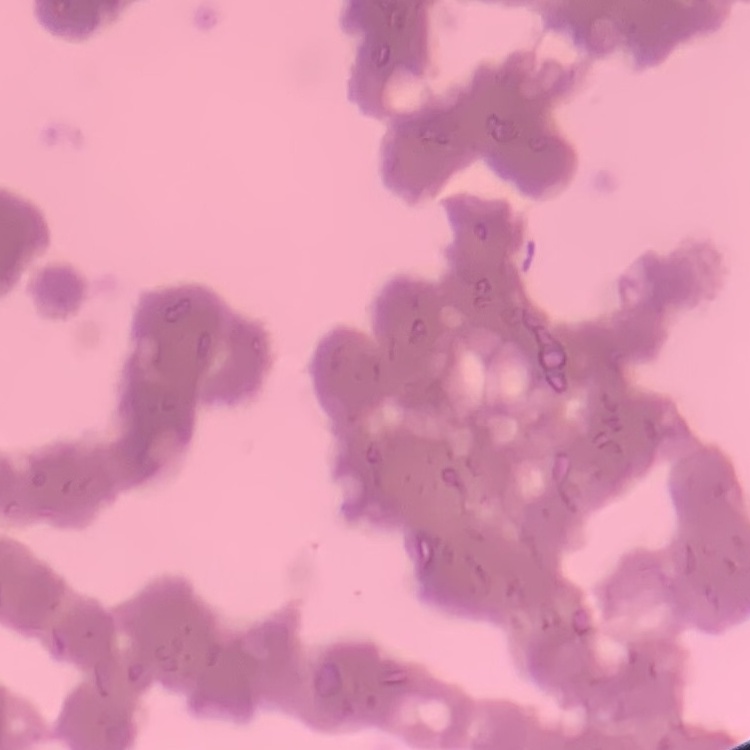

Summary:
  - Red blood cell morphology: rouleaux formation
  - Preparation: thin blood smear
  - Stain: Field's or Giemsa
  - Image type: square crop of a larger photomicrograph